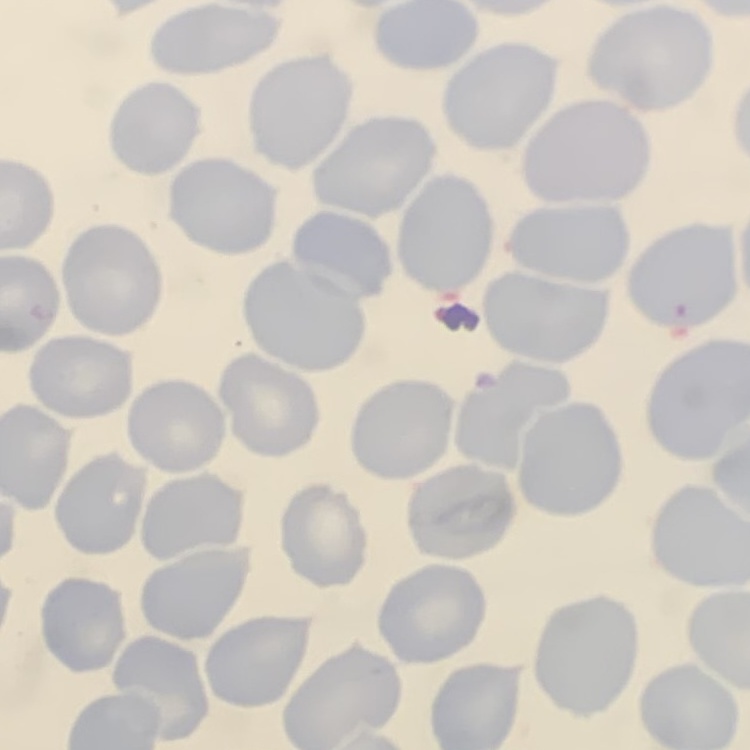

Summary:
  - Red blood cell morphology: no rouleaux formation
  - Image type: square crop of a larger photomicrograph
  - Stain: Field's or Giemsa
  - Preparation: thin blood smear